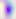
Summary:
  - Identification: Toxoplasma gondii
  - Magnification: 400x
  - Modality: micrograph